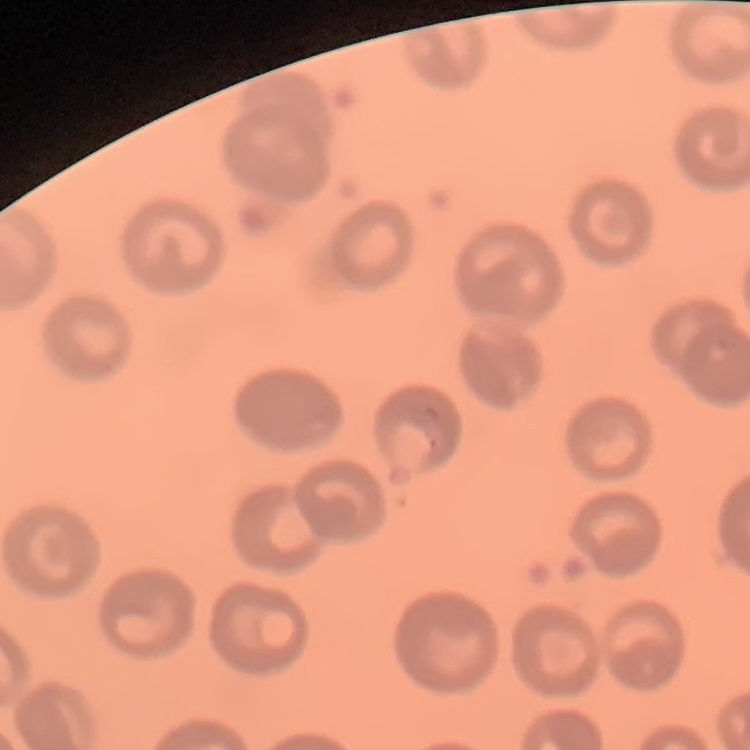 The red blood cells show no rouleaux formation. Square crop of a larger photomicrograph. Stained with either Field's or Giemsa. Thin blood smear.